Report the malaria status of this cell.
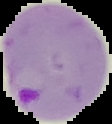
Parasitized.

image_size: 112×124 pixels
image_type: segmented cell region with the area outside set to black
preparation: thin blood smear